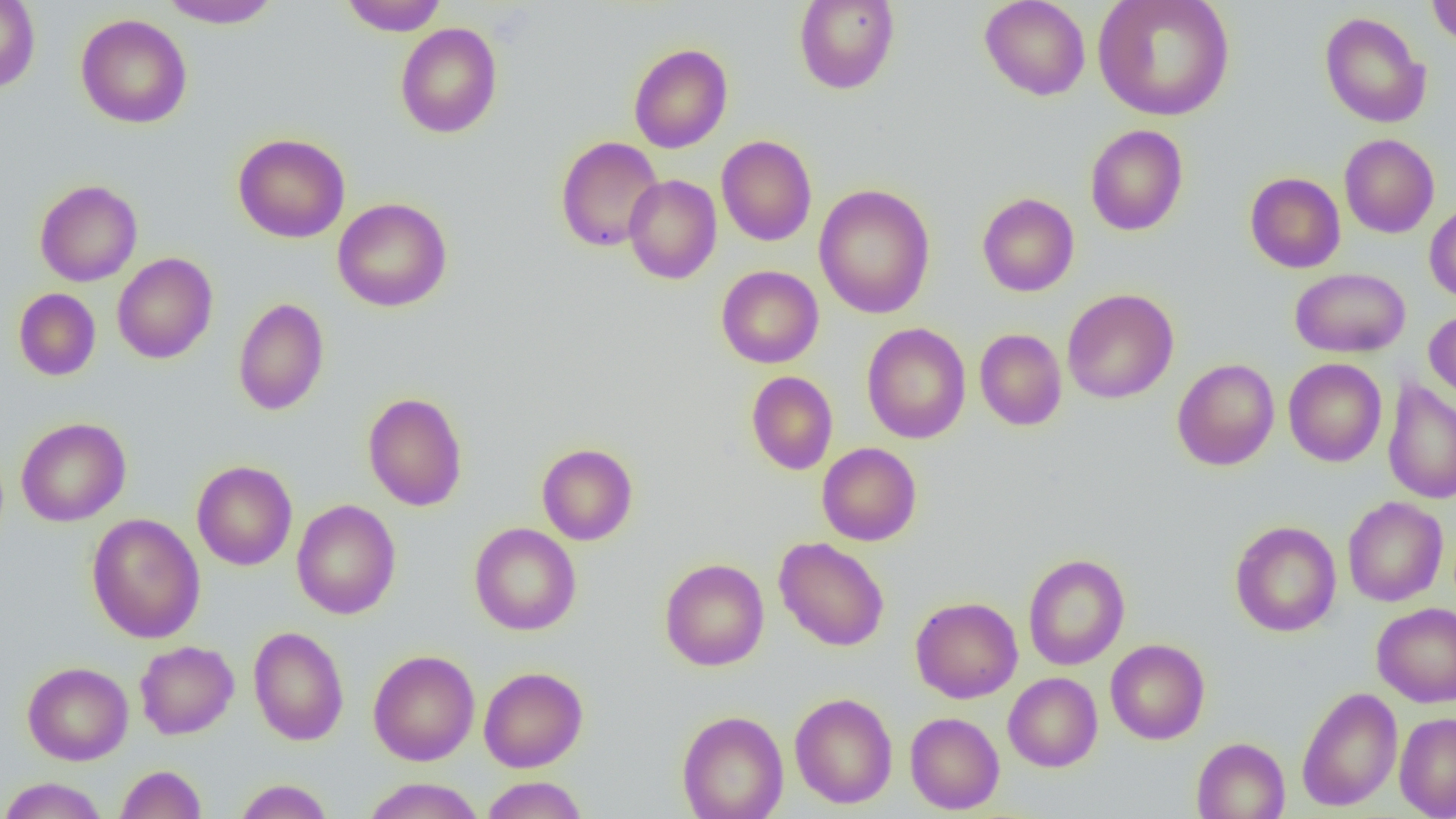

Approximate bounding boxes as named x1/y1/x2/y2 corners in pixels. Uninfected red blood cell locations: (x1=158, y1=0, x2=282, y2=29), (x1=340, y1=0, x2=447, y2=36), (x1=793, y1=0, x2=900, y2=94), (x1=979, y1=0, x2=1091, y2=101), (x1=1093, y1=0, x2=1235, y2=122), (x1=1427, y1=0, x2=1456, y2=47), (x1=0, y1=1, x2=40, y2=94), (x1=1319, y1=11, x2=1432, y2=128), (x1=75, y1=14, x2=192, y2=128), (x1=395, y1=23, x2=503, y2=138), (x1=629, y1=44, x2=732, y2=153), (x1=1085, y1=124, x2=1189, y2=236), (x1=232, y1=133, x2=350, y2=243), (x1=1339, y1=134, x2=1440, y2=238), (x1=716, y1=135, x2=817, y2=246), (x1=555, y1=136, x2=664, y2=252), (x1=1245, y1=172, x2=1345, y2=273), (x1=623, y1=174, x2=722, y2=284), (x1=34, y1=179, x2=142, y2=286), (x1=814, y1=184, x2=935, y2=319), (x1=977, y1=193, x2=1079, y2=297), (x1=332, y1=197, x2=452, y2=312), (x1=1424, y1=202, x2=1456, y2=302), (x1=112, y1=252, x2=218, y2=364), (x1=716, y1=265, x2=824, y2=368), (x1=1290, y1=267, x2=1411, y2=358), (x1=13, y1=288, x2=101, y2=381), (x1=1062, y1=288, x2=1179, y2=404), (x1=233, y1=297, x2=329, y2=416), (x1=1424, y1=309, x2=1456, y2=407), (x1=861, y1=323, x2=971, y2=444), (x1=975, y1=328, x2=1067, y2=431), (x1=1172, y1=358, x2=1279, y2=470), (x1=1283, y1=358, x2=1387, y2=466), (x1=746, y1=370, x2=838, y2=474), (x1=1382, y1=379, x2=1456, y2=504), (x1=363, y1=392, x2=467, y2=511), (x1=15, y1=417, x2=131, y2=526), (x1=817, y1=442, x2=922, y2=546), (x1=536, y1=443, x2=638, y2=545), (x1=191, y1=460, x2=297, y2=570), (x1=1342, y1=496, x2=1448, y2=606), (x1=291, y1=499, x2=401, y2=619), (x1=86, y1=513, x2=205, y2=643), (x1=1229, y1=520, x2=1341, y2=637), (x1=469, y1=522, x2=581, y2=636), (x1=774, y1=537, x2=890, y2=651), (x1=1022, y1=553, x2=1130, y2=670), (x1=659, y1=558, x2=769, y2=670), (x1=910, y1=597, x2=1023, y2=703), (x1=1371, y1=602, x2=1456, y2=707), (x1=248, y1=626, x2=348, y2=745), (x1=1106, y1=639, x2=1210, y2=744), (x1=135, y1=640, x2=239, y2=739), (x1=367, y1=650, x2=480, y2=765), (x1=22, y1=661, x2=134, y2=765), (x1=479, y1=666, x2=588, y2=772), (x1=1003, y1=672, x2=1103, y2=772), (x1=1296, y1=686, x2=1403, y2=811), (x1=789, y1=692, x2=898, y2=809), (x1=677, y1=710, x2=789, y2=819), (x1=905, y1=712, x2=1004, y2=814), (x1=1395, y1=712, x2=1456, y2=818), (x1=1191, y1=737, x2=1289, y2=819), (x1=115, y1=765, x2=206, y2=819), (x1=481, y1=776, x2=588, y2=818), (x1=0, y1=777, x2=108, y2=819), (x1=362, y1=777, x2=485, y2=819), (x1=233, y1=779, x2=333, y2=819). Slide-level diagnosis: negative for blood parasites. Optical microscopy. Captured at 1000x magnification. Image is 1456×819 pixels. Thin blood film. Single field of view.